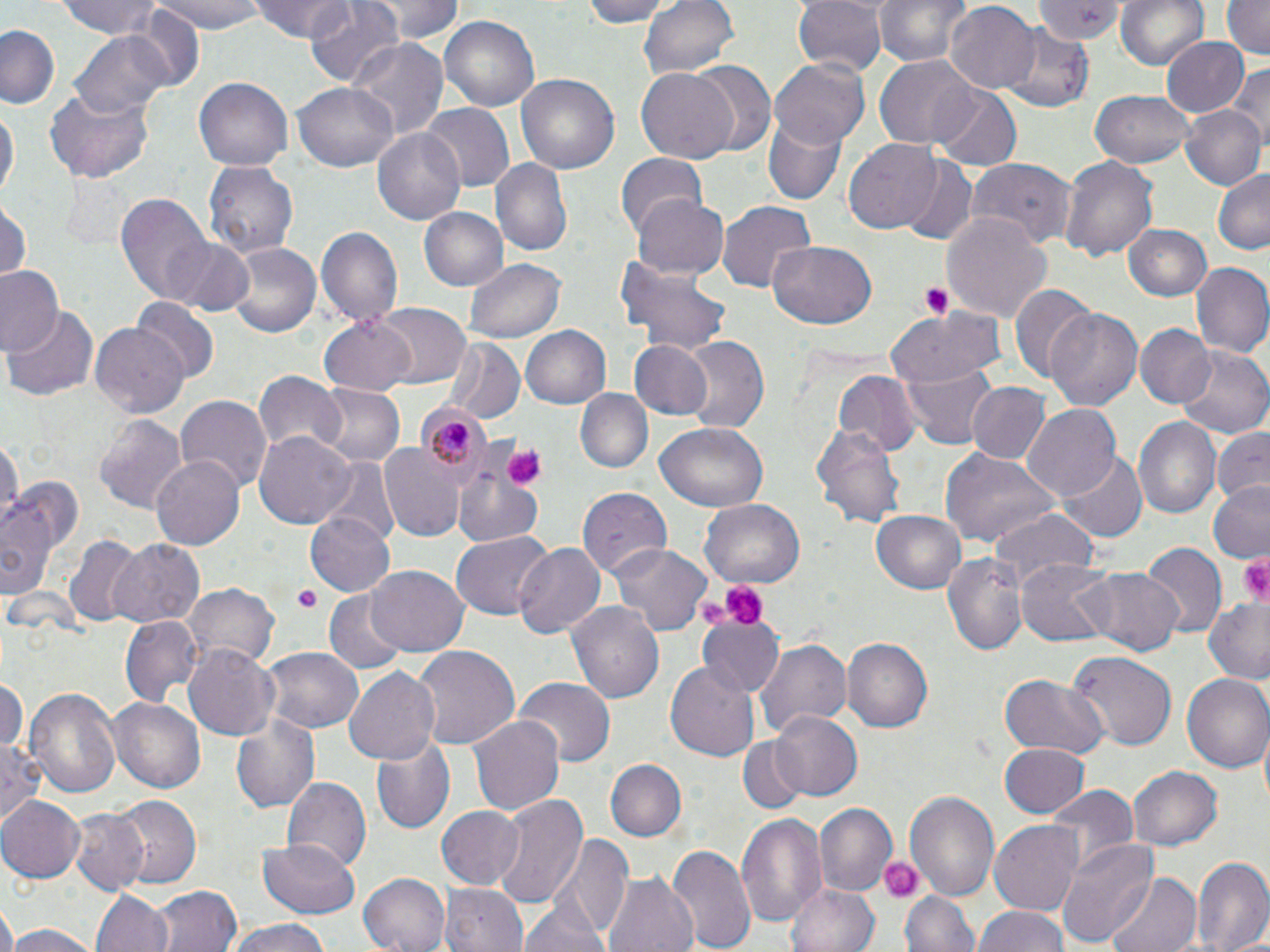

{
  "plasmodium_malariae_infected_red_blood_cell_locations": "approximate bounding boxes as (x1,y1)-(x2,y2) corner pairs in pixels: (415,402)-(491,484)",
  "slide_level_diagnosis": "Plasmodium malariae",
  "platelet_locations": "approximate bounding boxes as (x1,y1)-(x2,y2) corner pairs in pixels: (921,283)-(952,321), (501,443)-(548,489), (1241,554)-(1270,602), (712,578)-(769,630), (292,588)-(319,613), (697,600)-(729,633), (876,854)-(926,905)",
  "uninfected_red_blood_cell_locations": "approximate bounding boxes as (x1,y1)-(x2,y2) corner pairs in pixels: (56,0)-(168,39), (154,0)-(262,33), (251,0)-(360,41), (304,0)-(404,90), (369,0)-(465,45), (583,0)-(671,27), (640,0)-(740,80), (792,0)-(886,77), (871,0)-(972,65), (1033,0)-(1122,44), (1117,0)-(1208,70), (1220,0)-(1269,60), (946,2)-(1040,91), (124,6)-(204,91), (439,16)-(539,111), (1001,23)-(1098,112), (1,24)-(62,108), (72,29)-(176,121), (1163,37)-(1247,116), (346,39)-(449,138), (876,57)-(980,149), (687,58)-(776,153), (770,59)-(870,149), (1228,64)-(1270,161), (637,67)-(740,162), (514,72)-(620,178), (193,78)-(293,171), (293,78)-(398,171), (930,84)-(1022,172), (44,87)-(157,181), (1089,90)-(1197,169), (421,104)-(514,193), (1181,104)-(1265,192), (1,105)-(17,207), (764,115)-(847,205), (372,125)-(467,224), (845,139)-(944,233), (615,153)-(707,238), (1059,156)-(1158,263), (896,157)-(977,243), (967,157)-(1075,247), (490,159)-(572,256), (202,161)-(300,259), (1212,168)-(1270,256), (115,194)-(217,308), (632,196)-(727,279), (0,202)-(29,281), (717,202)-(816,296), (420,207)-(507,293), (940,211)-(1052,325), (1123,224)-(1213,301), (316,227)-(402,330), (165,237)-(255,318), (768,241)-(878,330), (228,242)-(321,337), (465,258)-(564,343), (614,261)-(734,357), (1190,263)-(1270,359), (0,264)-(64,356), (1009,284)-(1093,383), (131,300)-(217,386), (4,302)-(99,404), (373,303)-(470,390), (1048,304)-(1142,412), (887,311)-(1004,388), (320,315)-(418,394), (91,322)-(189,416), (522,325)-(610,409), (1137,326)-(1213,408), (678,337)-(769,434), (627,339)-(716,420), (442,340)-(525,426), (1176,349)-(1269,439), (898,364)-(996,449), (254,371)-(347,456), (834,372)-(921,457), (964,382)-(1052,465), (312,384)-(404,469), (576,390)-(651,474), (176,394)-(270,493), (1023,404)-(1120,502), (95,413)-(188,512), (1134,416)-(1221,518), (656,422)-(769,512), (811,424)-(906,530), (1211,426)-(1270,506), (254,432)-(358,528), (0,438)-(23,524), (379,442)-(464,540), (940,448)-(1057,548), (1057,451)-(1147,543), (151,455)-(244,551), (455,458)-(545,546), (319,459)-(400,549), (7,480)-(81,565), (1209,482)-(1270,562), (577,487)-(670,580), (1,495)-(59,603), (699,499)-(805,587), (871,510)-(969,594), (307,511)-(394,595), (988,511)-(1099,591), (450,532)-(552,619), (64,536)-(143,627), (106,539)-(207,629), (512,541)-(606,640), (609,542)-(710,637), (1139,545)-(1225,638), (939,552)-(1026,656), (1016,560)-(1117,647), (366,566)-(468,657), (1076,568)-(1183,656), (184,583)-(279,669), (326,591)-(409,670), (567,600)-(665,704), (1202,600)-(1270,685), (120,616)-(202,704), (698,616)-(780,698), (756,637)-(851,738), (842,639)-(933,732), (184,644)-(279,741), (259,645)-(364,734), (413,645)-(519,751), (1067,653)-(1175,752), (666,659)-(759,763), (342,665)-(441,764), (999,674)-(1110,759), (0,675)-(26,753), (1183,675)-(1270,775), (511,678)-(614,767), (24,684)-(122,803), (110,698)-(206,792), (769,710)-(863,802), (232,714)-(322,814), (469,714)-(564,816), (1,734)-(48,827), (372,736)-(457,835), (738,738)-(805,813), (998,743)-(1088,818), (605,759)-(686,842), (1128,765)-(1224,850), (281,776)-(370,873), (1045,784)-(1137,868), (905,790)-(1000,902), (492,792)-(586,912), (0,795)-(84,883), (111,795)-(202,887), (814,803)-(896,896), (436,806)-(526,889), (68,809)-(150,895), (738,812)-(827,930), (990,822)-(1082,913), (558,835)-(633,940), (260,837)-(360,915), (1056,838)-(1158,946), (667,844)-(756,952), (1190,855)-(1270,952), (359,872)-(452,952), (1105,872)-(1200,952), (605,874)-(697,952), (785,881)-(878,952), (440,883)-(530,952), (151,885)-(244,952), (90,887)-(175,952), (903,890)-(979,952), (519,897)-(614,952), (0,904)-(16,952), (973,906)-(1074,952), (224,919)-(330,952), (3,925)-(99,952)",
  "stain": "May-Grünwald-Giemsa",
  "preparation": "thin blood smear",
  "modality": "light microscopy",
  "image_size": "1270×952 pixels",
  "field_of_view": "one of a larger specimen",
  "magnification": "1000x"
}